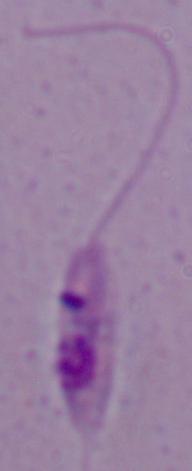
Summary:
  - Modality: photomicrograph
  - Magnification: 1000x
  - Identification: Leishmania